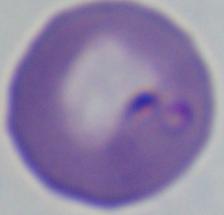

identification: Babesia
modality: micrograph
magnification: 1000x